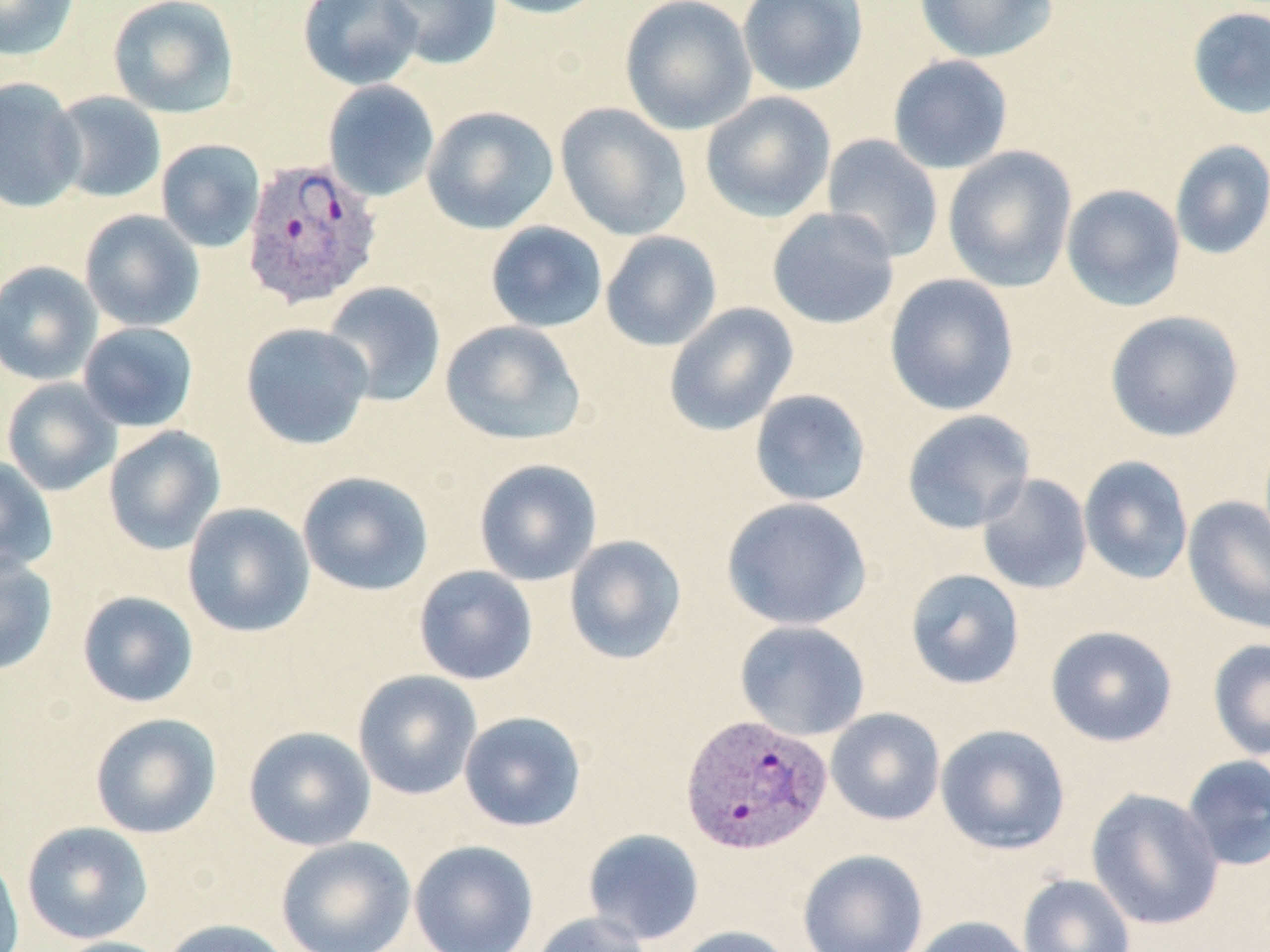 Approximate bounding boxes as (x1, y1, x2, y2) in pixels. Plasmodium vivax-infected red blood cell locations: (241, 156, 385, 311), (680, 714, 832, 856). Uninfected red blood cell locations: (0, 0, 81, 61), (107, 0, 240, 119), (298, 0, 424, 91), (381, 0, 502, 70), (476, 0, 610, 19), (619, 0, 757, 135), (737, 0, 868, 96), (914, 0, 1058, 63), (1186, 6, 1269, 119), (887, 54, 1014, 175), (0, 77, 85, 213), (323, 80, 440, 202), (49, 91, 167, 203), (700, 91, 836, 222), (555, 103, 692, 240), (422, 105, 559, 234), (821, 134, 944, 263), (155, 139, 266, 252), (1169, 140, 1270, 260), (943, 146, 1077, 292), (1061, 184, 1186, 312), (766, 207, 899, 330), (79, 209, 205, 332), (485, 221, 608, 333), (600, 231, 722, 352), (0, 260, 103, 385), (884, 273, 1020, 416), (321, 281, 446, 406), (664, 302, 799, 436), (1105, 310, 1244, 442), (440, 319, 586, 446), (78, 321, 199, 432), (240, 322, 374, 450), (1, 377, 122, 496), (749, 389, 872, 507), (901, 409, 1036, 534), (103, 426, 226, 555), (1078, 455, 1194, 585), (0, 456, 58, 575), (474, 458, 603, 586), (297, 471, 434, 596), (977, 473, 1093, 595), (1182, 495, 1270, 635), (721, 497, 873, 631), (182, 502, 315, 637), (564, 534, 687, 665), (0, 554, 58, 676), (413, 565, 537, 685), (905, 568, 1025, 690), (77, 590, 199, 708), (734, 620, 871, 741), (1045, 625, 1178, 747), (1207, 639, 1270, 760), (352, 670, 483, 800), (825, 708, 946, 826), (459, 710, 587, 832), (89, 712, 222, 839), (935, 724, 1071, 855), (243, 726, 376, 851), (1181, 754, 1270, 871), (1086, 788, 1225, 930), (21, 821, 154, 944), (582, 828, 705, 945), (276, 836, 416, 952), (409, 840, 539, 952), (0, 849, 25, 952), (798, 849, 928, 952), (1017, 873, 1136, 952), (529, 911, 653, 952), (908, 915, 1037, 952), (159, 918, 293, 952), (671, 925, 792, 952), (50, 936, 177, 952). Slide-level diagnosis: Plasmodium vivax. May-Grünwald-Giemsa stain. Thin blood film. Light microscopy. One field of a larger specimen. Captured at 1000x magnification. Image is 1270×952 pixels.